Locate every Plasmodium parasite and every leukocyte.
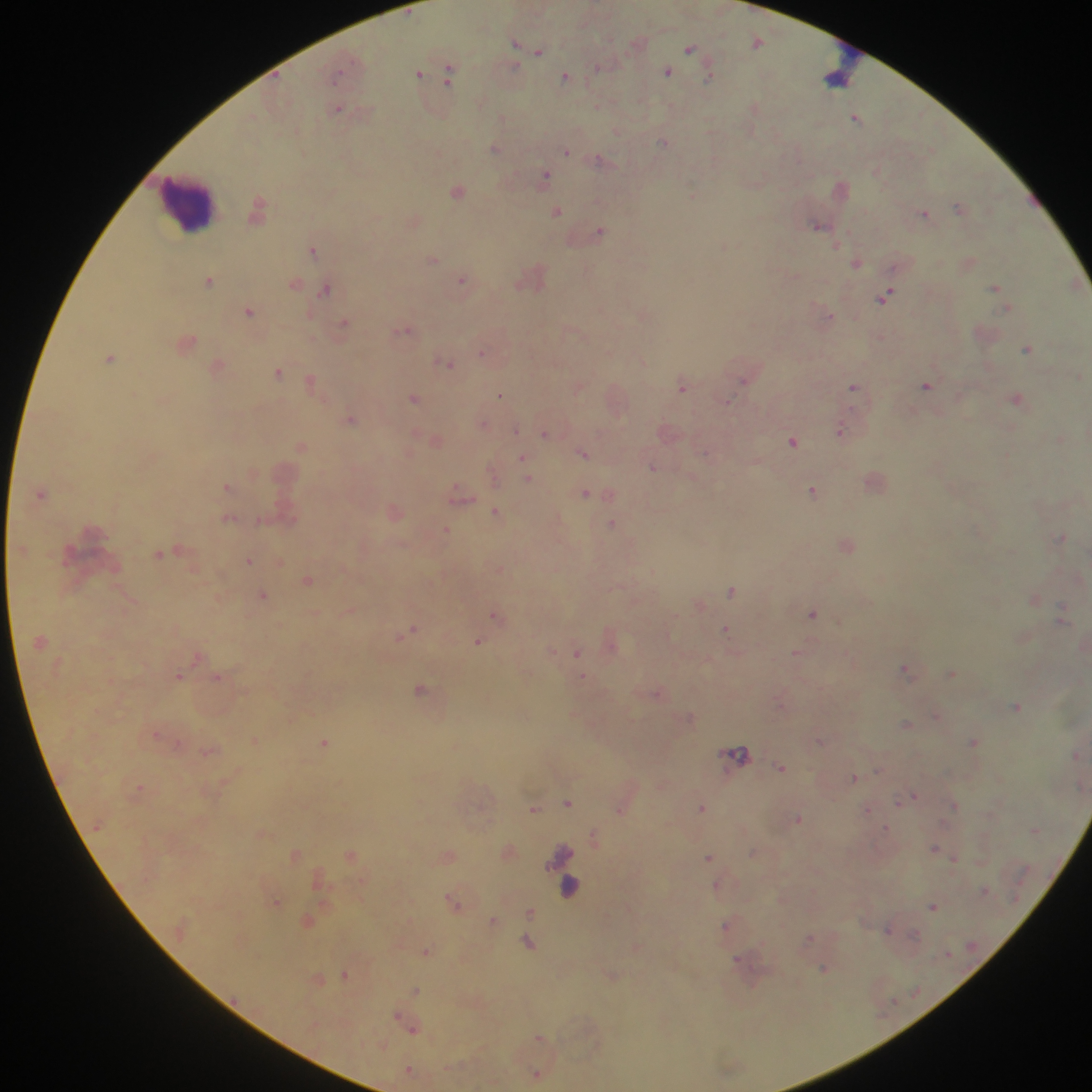

Approximate centers as (x, y) in pixels.
Plasmodium parasites: (757, 41), (515, 43), (690, 48), (539, 52), (513, 67), (667, 72), (339, 73), (418, 74), (448, 75), (565, 77), (708, 78), (597, 105), (338, 108), (754, 108), (502, 118), (856, 118), (617, 132), (663, 143), (496, 149), (566, 152), (599, 160), (544, 177), (458, 191), (692, 195), (958, 207), (258, 209), (557, 211), (925, 213), (818, 225), (600, 231), (725, 246), (313, 249), (433, 259), (856, 262), (462, 279), (209, 280), (294, 283), (994, 288), (326, 290), (885, 295), (249, 311), (831, 315), (343, 323), (404, 330), (188, 342), (1027, 349), (482, 353), (110, 358), (450, 364), (218, 366), (278, 372), (1080, 376), (743, 381), (311, 382), (926, 386), (853, 387), (578, 388), (682, 388), (499, 395), (414, 398), (1016, 399), (728, 401), (352, 420), (483, 423), (516, 430), (840, 430), (545, 434), (792, 441), (301, 446), (583, 453), (522, 457), (653, 467), (527, 478), (227, 487), (812, 490), (41, 493), (460, 493), (585, 494), (497, 512), (228, 518), (258, 521), (612, 524), (446, 530), (1062, 537), (159, 554), (249, 560), (308, 579), (731, 590), (263, 595), (1062, 609), (495, 614), (812, 614), (725, 630), (410, 631), (478, 642), (552, 651), (577, 652), (797, 652), (906, 669), (952, 673), (178, 675), (218, 677), (582, 678), (420, 689), (658, 693), (1017, 707), (936, 716), (906, 724), (157, 734), (820, 741), (974, 741), (324, 743), (739, 753), (781, 767), (854, 777), (914, 796), (567, 803), (955, 806), (702, 807), (533, 809), (620, 810), (867, 810), (798, 819), (887, 828), (1035, 830), (594, 836), (935, 848), (709, 857), (954, 860), (985, 890), (453, 903), (933, 906), (530, 911), (493, 921), (726, 926), (888, 930), (914, 935), (809, 939), (528, 943), (427, 951), (738, 960), (824, 969), (345, 975), (415, 990), (412, 1028), (540, 1037), (408, 1070), (536, 1073).
Leukocytes: (849, 66), (190, 207), (566, 874).

{
  "country": "Ghana",
  "field_of_view": "single",
  "preparation": "thick blood smear",
  "image_size": "1092×1092 pixels",
  "capture": "mobile-phone photograph through a microscope"
}